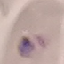
Malaria status: parasitized. Thin smear of blood. Acquired by smartphone through the microscope eyepiece. Giemsa-stained preparation. Cell patch, automatically extracted from a larger field of view and resized to 64 × 64 pixels.